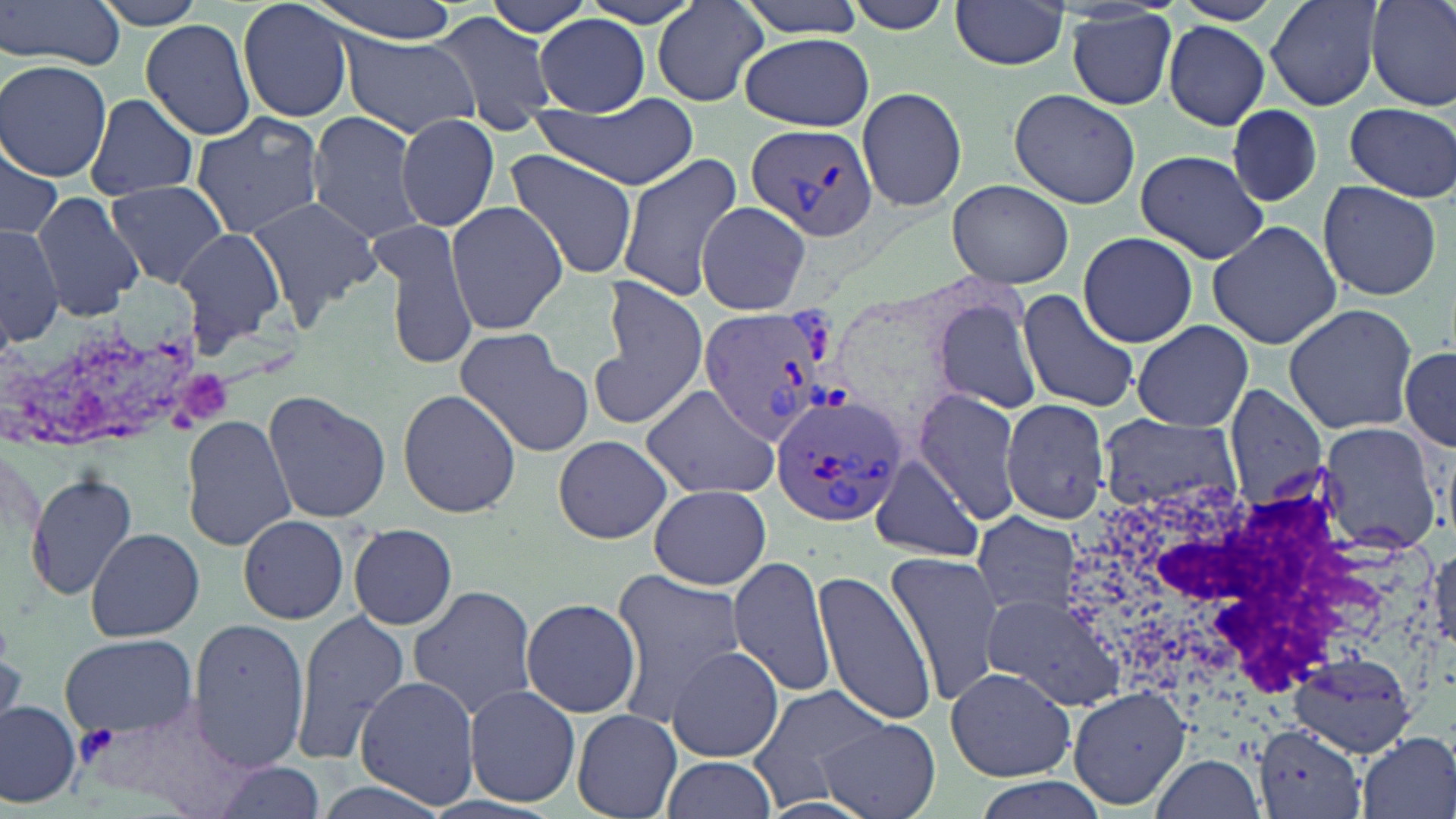

Summary:
  - Coordinate format: approximate bounding boxes as (x1, y1, x2, y2) in pixels
  - Plasmodium vivax-infected red blood cell locations: (746, 122, 880, 244), (695, 306, 827, 440), (769, 388, 907, 530), (68, 704, 237, 815)
  - White blood cell locations: (1060, 467, 1440, 740)
  - Uninfected red blood cell locations: (1, 0, 129, 74), (89, 0, 217, 29), (302, 0, 466, 41), (481, 0, 597, 38), (574, 0, 708, 30), (733, 0, 873, 36), (1172, 0, 1285, 25), (1264, 0, 1384, 111), (1366, 0, 1456, 111), (237, 1, 356, 122), (837, 1, 958, 33), (950, 1, 1071, 70), (653, 3, 769, 107), (1066, 10, 1178, 110), (433, 11, 556, 132), (535, 15, 651, 115), (139, 19, 257, 139), (1163, 21, 1271, 128), (739, 32, 875, 131), (342, 34, 479, 137), (1, 59, 112, 181), (856, 86, 968, 212), (1009, 88, 1141, 209), (83, 94, 198, 202), (530, 96, 700, 189), (1343, 103, 1456, 200), (1225, 107, 1325, 206), (306, 110, 429, 246), (190, 114, 326, 236), (395, 114, 502, 232), (0, 141, 64, 244), (503, 149, 641, 281), (1136, 149, 1271, 264), (615, 154, 744, 301), (947, 178, 1075, 288), (1316, 179, 1443, 301), (105, 180, 228, 287), (33, 190, 143, 319), (246, 195, 381, 324), (695, 200, 811, 314), (446, 202, 567, 335), (1206, 219, 1344, 351), (380, 223, 477, 373), (0, 225, 65, 346), (175, 228, 288, 349), (1077, 232, 1199, 348), (590, 289, 709, 427), (1017, 289, 1141, 414), (929, 296, 1045, 415), (1283, 304, 1419, 435), (1132, 320, 1253, 431), (453, 329, 592, 456), (1400, 344, 1455, 452), (639, 382, 780, 500), (1225, 387, 1330, 508), (398, 389, 521, 519), (913, 389, 1023, 525), (262, 390, 392, 523), (1002, 400, 1114, 523), (182, 415, 296, 550), (1096, 417, 1244, 515), (1316, 420, 1445, 553), (553, 434, 672, 543), (870, 454, 986, 563), (26, 470, 138, 600), (650, 483, 771, 590), (969, 509, 1084, 623), (238, 513, 350, 625), (350, 524, 457, 631), (86, 527, 204, 642), (1429, 543, 1455, 653), (885, 551, 1002, 705), (728, 557, 837, 699), (812, 571, 937, 727), (611, 572, 745, 718), (406, 584, 540, 722), (985, 593, 1126, 712), (521, 597, 642, 717), (289, 609, 412, 769), (190, 618, 311, 771), (62, 635, 196, 737), (666, 645, 785, 763), (1287, 647, 1420, 757), (945, 666, 1076, 782), (354, 675, 480, 810), (751, 684, 893, 800), (1068, 684, 1194, 810), (464, 685, 581, 807), (0, 699, 80, 806), (570, 708, 682, 819), (817, 718, 940, 819), (1354, 731, 1455, 819), (1150, 755, 1265, 817), (662, 756, 778, 818), (209, 761, 326, 819)
  - Slide-level diagnosis: Plasmodium vivax
  - Field of view: single
  - Image size: 1456×819 pixels
  - Modality: optical microscopy
  - Magnification: 1000x
  - Stain: May-Grünwald-Giemsa
  - Preparation: thin blood smear